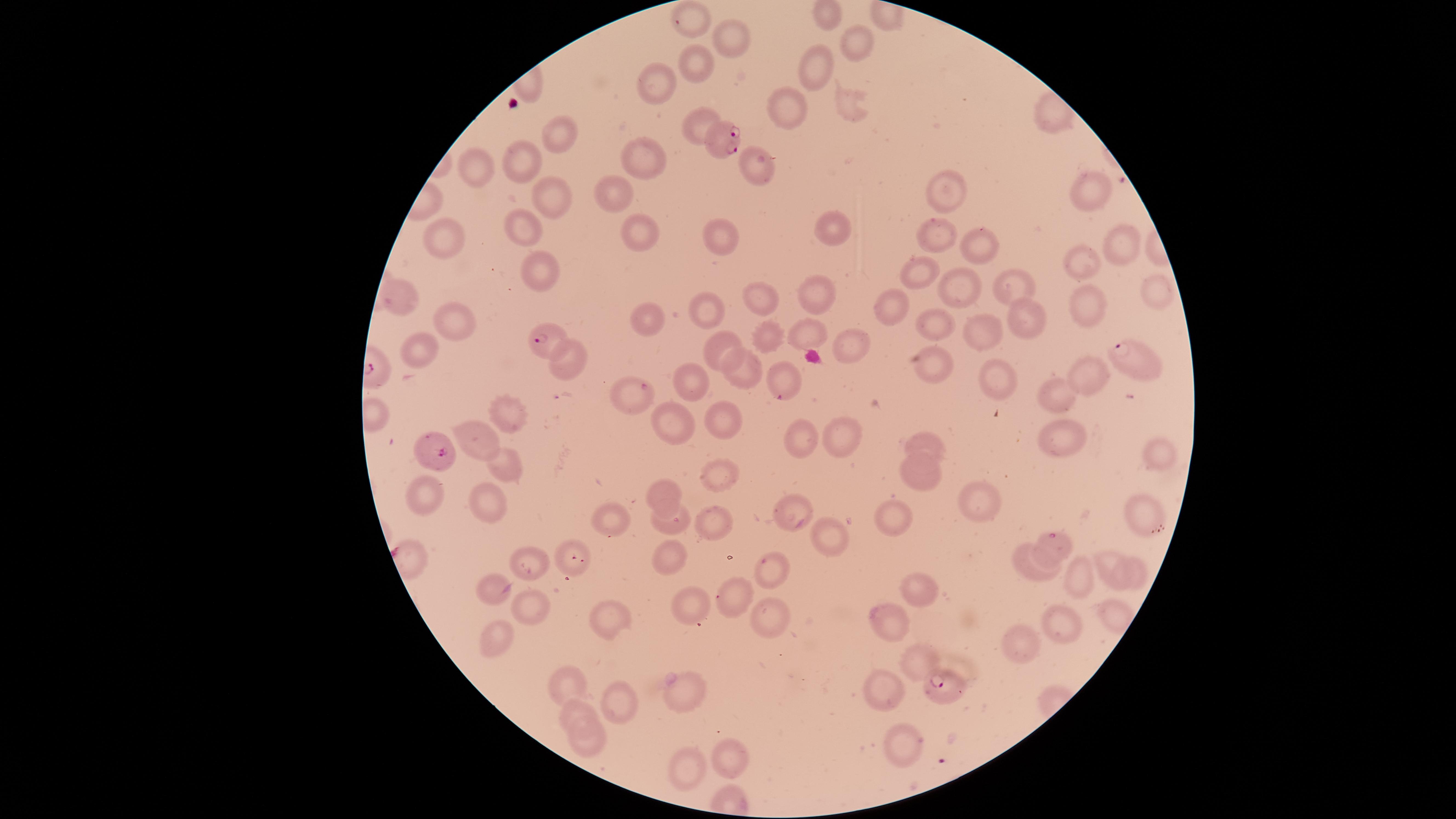

image size = 1456×819 pixels
preparation = thin smear of blood
stain = Giemsa
field of view = single
uninfected red blood cells = approximate marker points as (x, y) in pixels: (837, 9), (689, 19), (722, 38), (861, 39), (704, 64), (817, 67), (655, 80), (790, 107), (699, 129), (556, 140), (647, 160), (758, 160), (530, 161), (480, 168), (945, 194), (614, 195), (555, 196), (1080, 196), (829, 224), (524, 225), (640, 232), (934, 232), (443, 234), (723, 235), (979, 241), (1124, 241), (1076, 270), (920, 272), (541, 282), (1015, 286), (959, 287), (400, 288), (817, 291), (1157, 291), (770, 299), (1095, 306), (1029, 311), (701, 312), (891, 314), (455, 323), (648, 323), (933, 324), (763, 329), (801, 336), (720, 344), (851, 344), (421, 349), (572, 359), (935, 365), (1089, 367), (744, 371), (697, 377), (995, 377), (1060, 393), (510, 410), (664, 419), (724, 423), (842, 432), (481, 436), (800, 438), (1065, 439), (927, 442), (1159, 457), (502, 469), (916, 474), (716, 477), (666, 488), (427, 495), (982, 496), (484, 498), (795, 509), (1144, 510), (900, 513), (610, 519), (663, 521), (711, 525), (833, 538), (529, 558), (668, 562), (1108, 563), (1028, 573), (1137, 573), (1072, 574), (770, 575), (498, 583), (915, 585), (693, 598), (733, 602), (533, 609), (1063, 617), (763, 619), (613, 620), (892, 622), (494, 642), (1028, 643), (919, 650), (562, 682), (686, 690), (614, 702), (885, 702), (577, 715), (906, 742), (583, 748), (734, 755), (684, 763)
species = Plasmodium falciparum
capture = smartphone photograph through the microscope eyepiece
parasitized red blood cells = approximate marker points as (x, y) in pixels: (723, 138), (551, 342), (1136, 362), (782, 382), (631, 393), (437, 449), (1052, 541), (573, 558), (939, 688)
presence = malaria parasites detected
visible region = circular